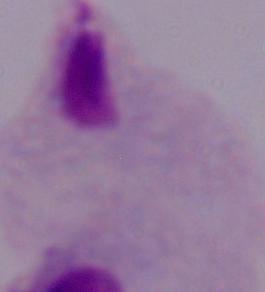
{
  "modality": "micrograph",
  "magnification": "1000x",
  "identification": "trichomonad"
}